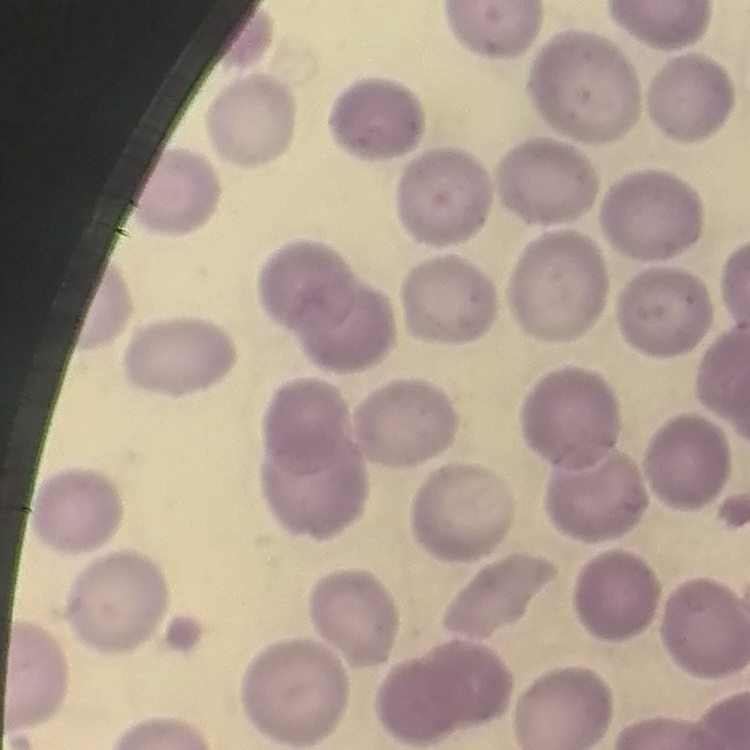 The erythrocytes show no rouleaux formation. Square crop of a larger photomicrograph. Stained with either Field's or Giemsa. Thin blood film.